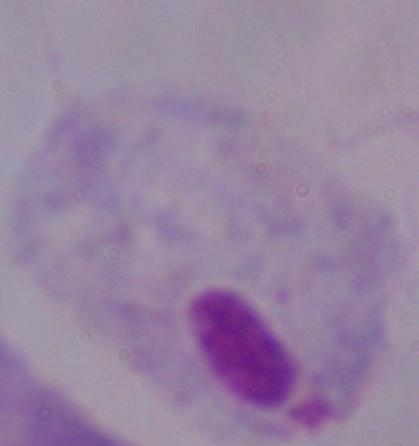

A trichomonad is seen. 1000x magnification. Micrograph.